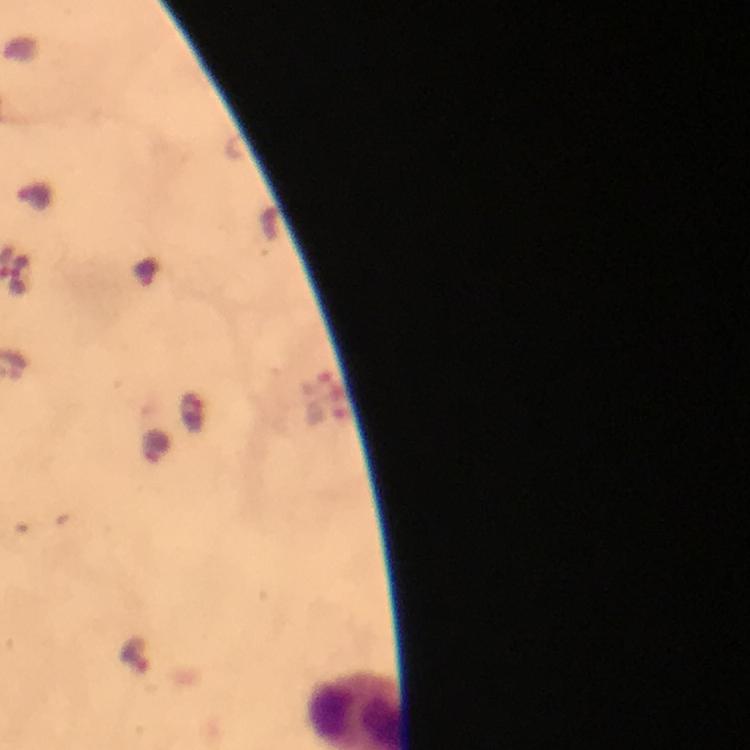

cropped from = one field of view
magnification = 100x
immersion oil = used
image size = 750×750 pixels
stain = Giemsa
malaria parasite locations = approximate centers as (x, y) in pixels: (136, 655)
context = from a malaria diagnostic workup
preparation = thick blood film
capture = smartphone mounted on the microscope